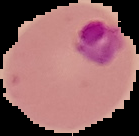 The area outside the segmented cell region is set to black. From a thin blood smear. Image is 139×136 pixels. Result: malaria parasites detected.